Assess the morphology of the red blood cells.
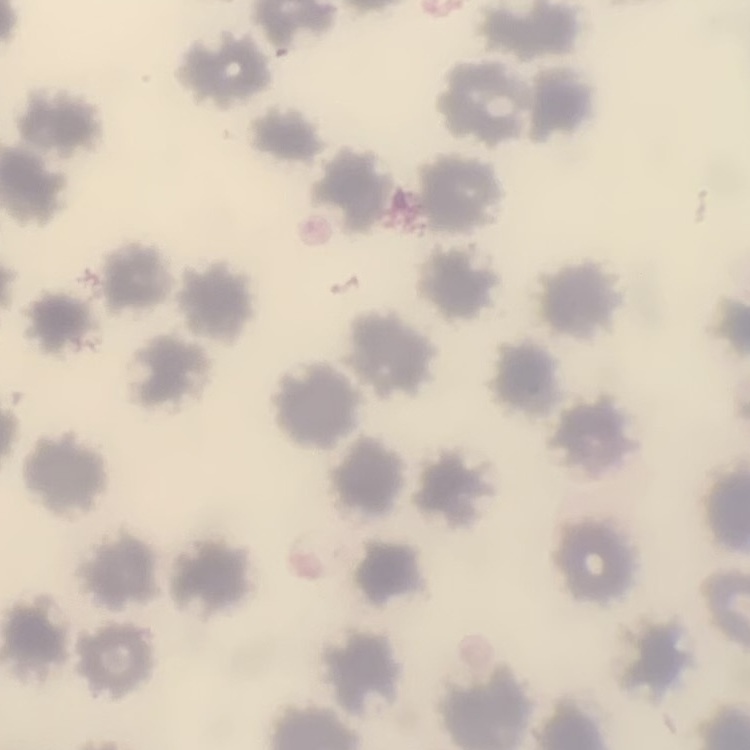

No rouleaux formation.

Stained with either Field's or Giemsa. One tile cut from a larger photomicrograph. Thin blood film.